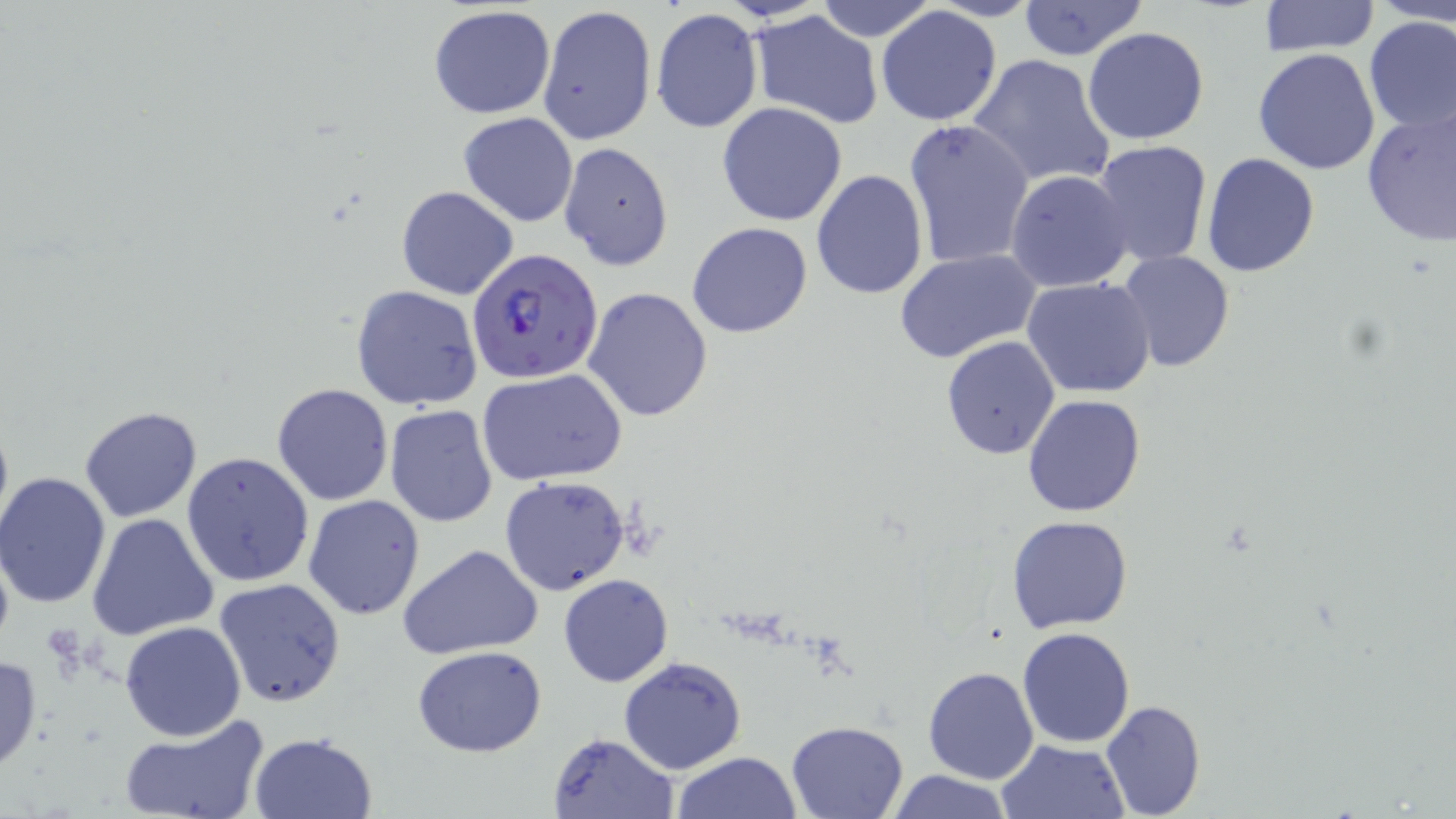 Approximate bounding boxes as named x1/y1/x2/y2 corners in pixels. Plasmodium falciparum-infected red blood cell locations: (x1=465, y1=248, x2=603, y2=385). Uninfected red blood cell locations: (x1=813, y1=0, x2=939, y2=42), (x1=1018, y1=0, x2=1149, y2=63), (x1=1260, y1=0, x2=1380, y2=55), (x1=1371, y1=0, x2=1454, y2=26), (x1=429, y1=4, x2=557, y2=120), (x1=539, y1=5, x2=657, y2=143), (x1=876, y1=7, x2=1004, y2=127), (x1=651, y1=8, x2=763, y2=135), (x1=748, y1=11, x2=885, y2=129), (x1=1361, y1=16, x2=1456, y2=135), (x1=1082, y1=27, x2=1212, y2=146), (x1=1254, y1=48, x2=1382, y2=176), (x1=968, y1=54, x2=1115, y2=189), (x1=717, y1=102, x2=848, y2=226), (x1=1360, y1=105, x2=1456, y2=248), (x1=458, y1=112, x2=579, y2=227), (x1=904, y1=118, x2=1035, y2=271), (x1=1093, y1=140, x2=1213, y2=266), (x1=559, y1=143, x2=674, y2=270), (x1=1202, y1=152, x2=1321, y2=277), (x1=811, y1=169, x2=927, y2=301), (x1=1006, y1=169, x2=1135, y2=291), (x1=396, y1=185, x2=519, y2=301), (x1=687, y1=222, x2=813, y2=339), (x1=893, y1=249, x2=1041, y2=362), (x1=1117, y1=249, x2=1236, y2=371), (x1=1023, y1=277, x2=1156, y2=399), (x1=350, y1=285, x2=484, y2=411), (x1=583, y1=286, x2=714, y2=423), (x1=940, y1=336, x2=1062, y2=460), (x1=475, y1=369, x2=627, y2=487), (x1=271, y1=383, x2=394, y2=506), (x1=1022, y1=393, x2=1145, y2=517), (x1=384, y1=405, x2=498, y2=528), (x1=77, y1=406, x2=203, y2=523), (x1=182, y1=452, x2=314, y2=589), (x1=1, y1=473, x2=114, y2=611), (x1=500, y1=474, x2=630, y2=596), (x1=302, y1=494, x2=425, y2=620), (x1=88, y1=514, x2=220, y2=643), (x1=1006, y1=515, x2=1135, y2=633), (x1=398, y1=544, x2=544, y2=661), (x1=558, y1=574, x2=674, y2=688), (x1=214, y1=577, x2=346, y2=707), (x1=120, y1=620, x2=246, y2=741), (x1=1017, y1=628, x2=1137, y2=747), (x1=412, y1=644, x2=548, y2=757), (x1=0, y1=653, x2=43, y2=772), (x1=618, y1=656, x2=747, y2=774), (x1=922, y1=666, x2=1038, y2=785), (x1=1099, y1=699, x2=1206, y2=818), (x1=117, y1=712, x2=270, y2=819), (x1=785, y1=720, x2=910, y2=817), (x1=249, y1=731, x2=377, y2=818), (x1=548, y1=732, x2=678, y2=818), (x1=995, y1=738, x2=1131, y2=818), (x1=671, y1=752, x2=804, y2=818), (x1=884, y1=768, x2=1015, y2=819). Slide-level diagnosis: Plasmodium falciparum. May-Grünwald-Giemsa stain. Single field of view. Captured at 1000x magnification. Thin blood smear. Optical microscopy. Image is 1456×819 pixels.